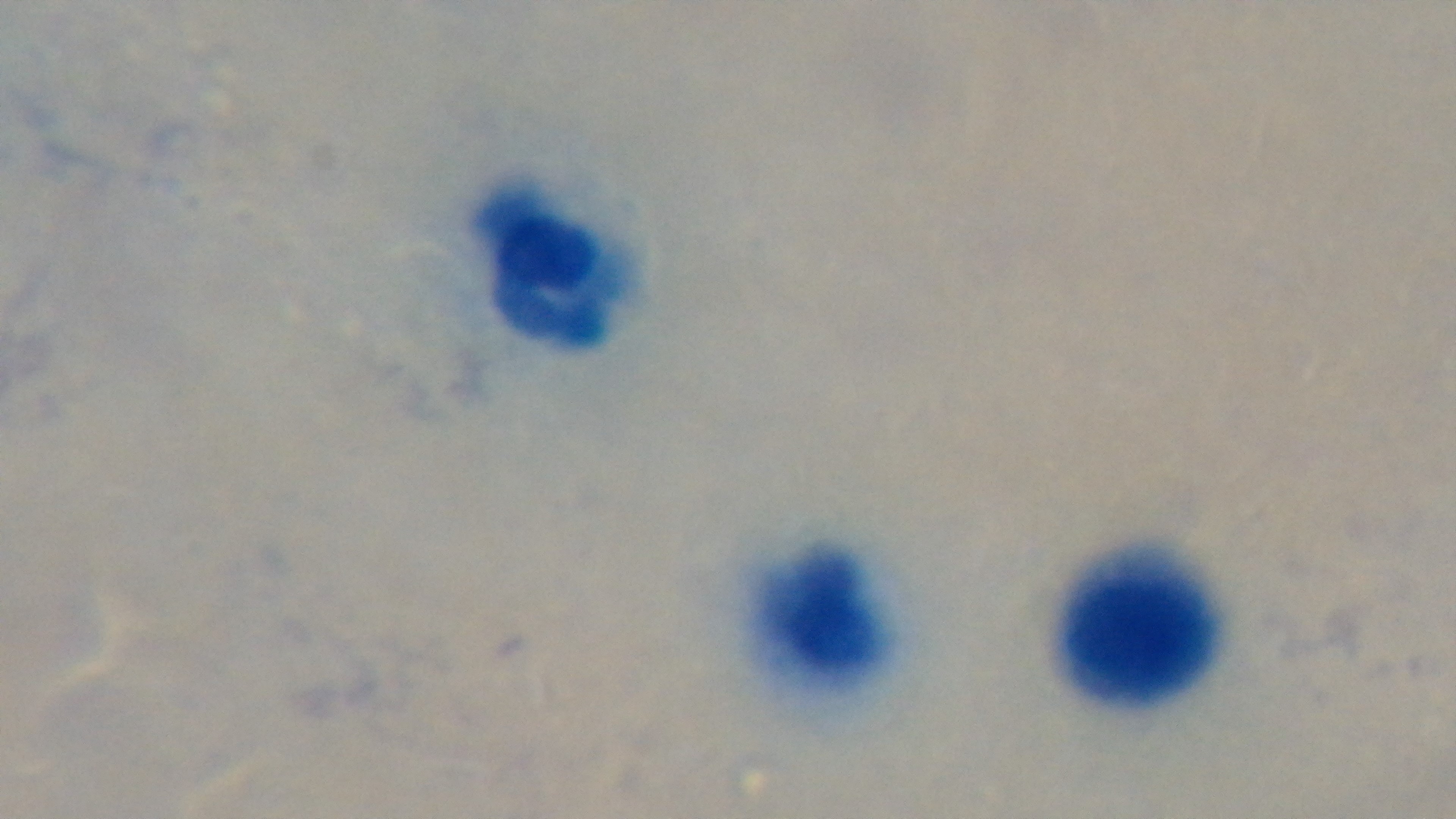
Malaria status: negative. Giemsa stain. Mounted 4K digital camera. One field from the slide. Photomicrograph. Preparation: thick blood film. 100x oil-immersion objective.